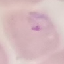

result: malaria parasites identified
stain: Giemsa
preparation: thin blood film
capture: smartphone camera at the microscope eyepiece
image_type: cell patch, automatically extracted from a larger field of view and resized to 64 × 64 pixels